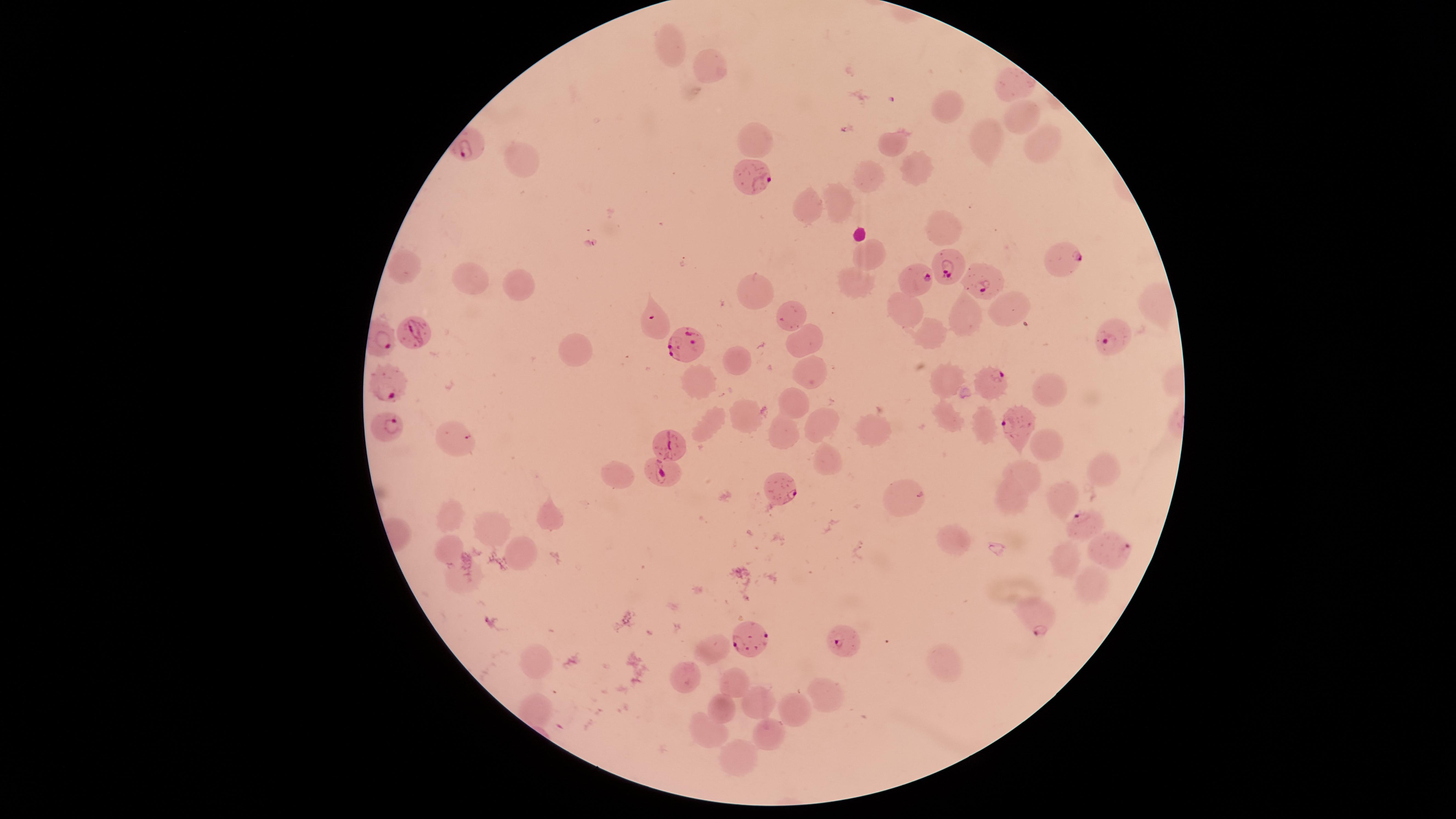 Approximate marker points as {x, y} in pixels. Parasitized RBCs: {749, 177}, {1066, 258}, {949, 268}, {921, 279}, {985, 283}, {654, 322}, {414, 333}, {1113, 337}, {687, 346}, {991, 381}, {388, 383}, {385, 424}, {1017, 425}, {672, 439}, {663, 470}, {778, 487}, {1080, 522}, {1106, 543}, {1037, 616}, {752, 632}, {850, 641}. Uninfected RBCs: {674, 43}, {710, 65}, {1019, 86}, {951, 108}, {1017, 118}, {986, 134}, {756, 135}, {1037, 141}, {892, 142}, {519, 157}, {917, 165}, {867, 178}, {837, 204}, {807, 207}, {942, 226}, {868, 255}, {408, 266}, {476, 274}, {850, 280}, {514, 285}, {753, 289}, {1161, 298}, {909, 306}, {1015, 312}, {789, 315}, {962, 318}, {806, 338}, {935, 339}, {574, 349}, {735, 360}, {805, 370}, {947, 380}, {697, 383}, {1048, 388}, {795, 404}, {742, 415}, {822, 417}, {703, 425}, {872, 428}, {779, 430}, {459, 434}, {1046, 447}, {824, 462}, {1025, 469}, {1106, 471}, {615, 475}, {910, 493}, {1007, 496}, {1059, 496}, {546, 512}, {450, 514}, {493, 524}, {962, 540}, {447, 542}, {521, 552}, {1066, 557}, {460, 576}, {1091, 591}, {714, 653}, {533, 660}, {938, 661}, {681, 674}, {735, 679}, {827, 690}, {757, 704}, {723, 706}, {793, 706}, {773, 730}, {707, 733}, {738, 757}. Smartphone photograph through the microscope eyepiece. Circular visible region. Thin blood film. Image is 1456×819 pixels. Species: Plasmodium falciparum. One field of view of the specimen. Giemsa-stained preparation. Presence: malaria parasites seen.